Assess this cell for malaria.
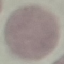

Uninfected.

Summary:
  - Capture: smartphone camera at the microscope eyepiece
  - Preparation: thin blood film
  - Stain: Giemsa
  - Image type: cell patch, automatically extracted from a larger field of view and resized to 64 × 64 pixels